Assess the background quality.
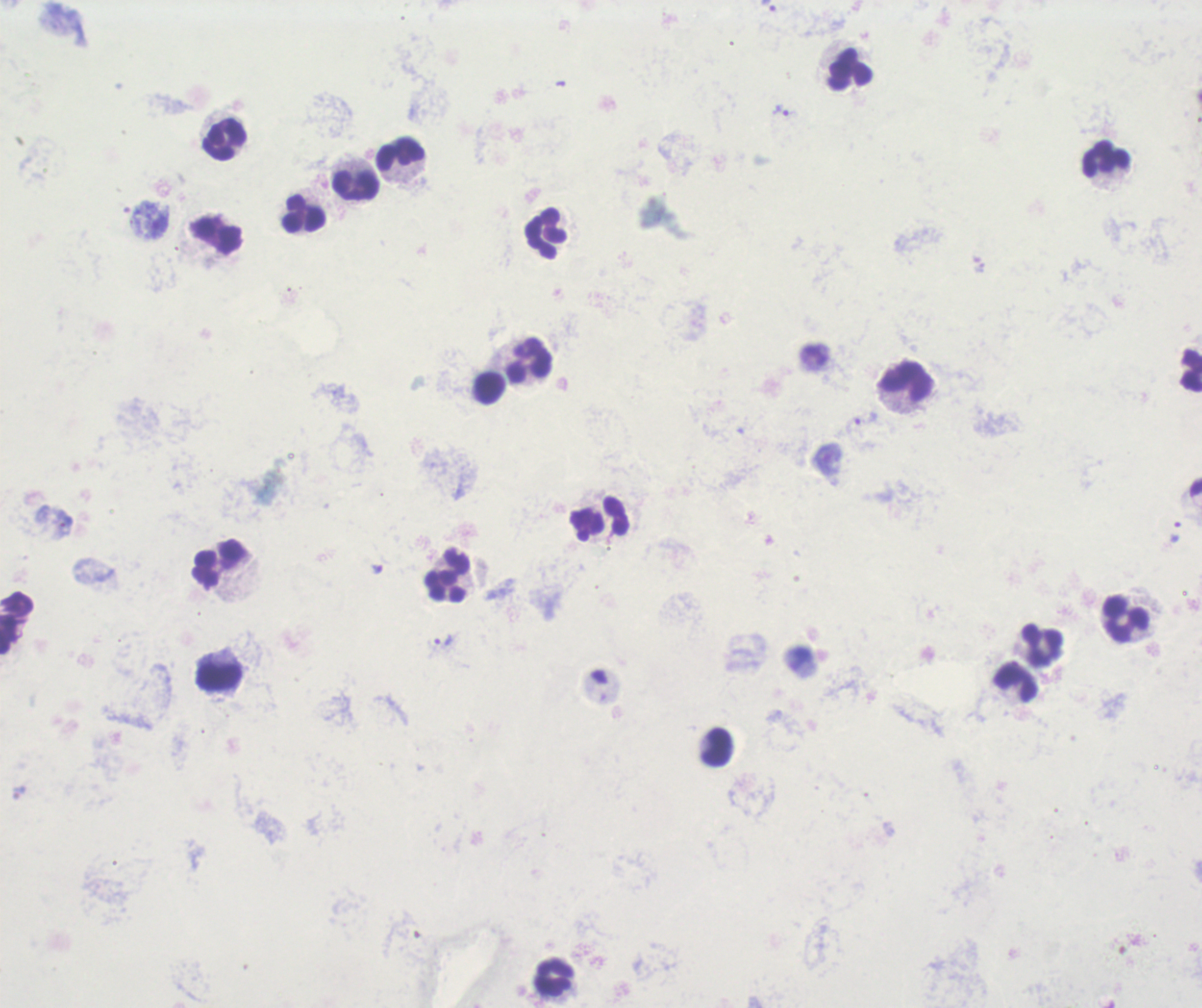
Unsatisfactory.

coordinate format = approximate centers as {x, y} in pixels
leukocyte locations = {848, 69}, {224, 142}, {400, 152}, {1105, 156}, {357, 185}, {305, 215}, {547, 232}, {216, 235}, {530, 361}, {908, 382}, {489, 388}, {617, 518}, {219, 564}, {447, 574}, {1124, 618}, {1043, 645}, {217, 677}, {1019, 682}, {716, 748}, {553, 977}
trophozoite locations = {767, 7}, {783, 111}, {442, 641}, {18, 790}
context = previously used in an actual diagnosis
field of view = single
image size = 1202×1008 pixels
stain = Romanowsky
result = positive for malaria parasites
preparation = thick smear of blood
magnification = 100x